Locate leukocytes (white blood cells).
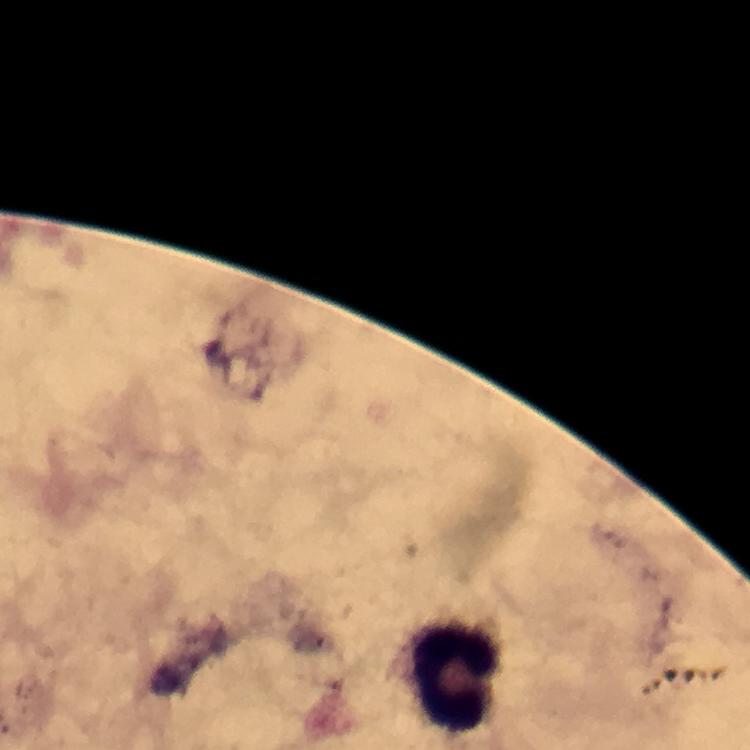
Approximate centers as (x, y) in pixels.
Leukocytes: (459, 673).

malaria parasites = none seen
image size = 750×750 pixels
magnification = 100x
stain = Giemsa
immersion oil = applied
cropped from = one field of view
preparation = thick smear
context = from a malaria diagnostic workup
capture = smartphone photograph through a microscope